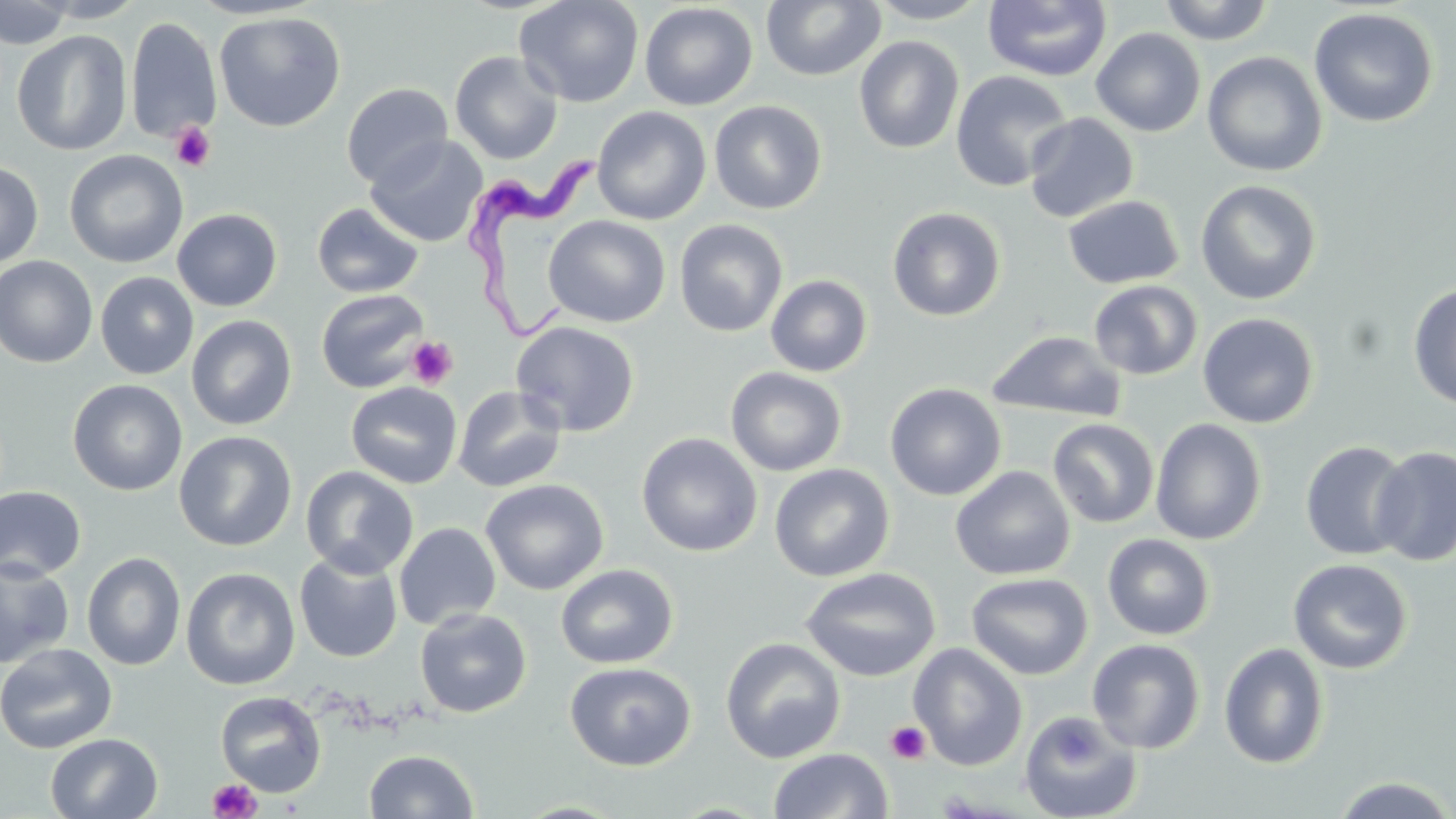
Approximate bounding boxes as named x1/y1/x2/y2 corners in pixels. Platelet locations: (x1=170, y1=121, x2=217, y2=171), (x1=406, y1=337, x2=457, y2=389), (x1=885, y1=720, x2=931, y2=764), (x1=208, y1=778, x2=262, y2=819). Trypanosoma brucei locations: (x1=460, y1=139, x2=609, y2=353). Uninfected red blood cell locations: (x1=0, y1=0, x2=75, y2=49), (x1=32, y1=0, x2=147, y2=23), (x1=514, y1=0, x2=645, y2=108), (x1=760, y1=0, x2=886, y2=82), (x1=865, y1=0, x2=994, y2=25), (x1=982, y1=0, x2=1112, y2=83), (x1=1156, y1=0, x2=1276, y2=45), (x1=639, y1=2, x2=758, y2=111), (x1=1308, y1=6, x2=1439, y2=129), (x1=213, y1=11, x2=346, y2=133), (x1=125, y1=16, x2=222, y2=143), (x1=1091, y1=27, x2=1206, y2=137), (x1=11, y1=30, x2=132, y2=155), (x1=853, y1=35, x2=964, y2=154), (x1=1091, y1=37, x2=1325, y2=154), (x1=450, y1=50, x2=563, y2=163), (x1=1202, y1=51, x2=1327, y2=177), (x1=950, y1=70, x2=1074, y2=192), (x1=341, y1=82, x2=453, y2=189), (x1=709, y1=100, x2=827, y2=214), (x1=592, y1=106, x2=711, y2=225), (x1=1023, y1=113, x2=1139, y2=223), (x1=365, y1=135, x2=487, y2=248), (x1=64, y1=150, x2=188, y2=268), (x1=0, y1=161, x2=43, y2=270), (x1=1195, y1=179, x2=1322, y2=305), (x1=1062, y1=195, x2=1184, y2=289), (x1=311, y1=202, x2=424, y2=298), (x1=887, y1=206, x2=1007, y2=322), (x1=172, y1=208, x2=282, y2=312), (x1=543, y1=215, x2=671, y2=328), (x1=674, y1=219, x2=789, y2=337), (x1=0, y1=256, x2=98, y2=368), (x1=95, y1=272, x2=199, y2=379), (x1=765, y1=274, x2=872, y2=377), (x1=1088, y1=280, x2=1203, y2=381), (x1=1407, y1=283, x2=1456, y2=411), (x1=316, y1=288, x2=430, y2=393), (x1=1197, y1=312, x2=1320, y2=428), (x1=186, y1=315, x2=297, y2=431), (x1=511, y1=320, x2=640, y2=437), (x1=985, y1=330, x2=1127, y2=423), (x1=726, y1=367, x2=847, y2=476), (x1=68, y1=378, x2=187, y2=496), (x1=346, y1=382, x2=463, y2=488), (x1=884, y1=382, x2=1007, y2=501), (x1=452, y1=386, x2=566, y2=493), (x1=1150, y1=417, x2=1267, y2=546), (x1=1047, y1=418, x2=1160, y2=528), (x1=174, y1=430, x2=297, y2=552), (x1=636, y1=432, x2=762, y2=557), (x1=1299, y1=439, x2=1414, y2=561), (x1=1369, y1=445, x2=1456, y2=566), (x1=769, y1=463, x2=895, y2=582), (x1=950, y1=465, x2=1076, y2=581), (x1=301, y1=466, x2=419, y2=579), (x1=480, y1=478, x2=609, y2=595), (x1=0, y1=486, x2=86, y2=582), (x1=394, y1=522, x2=501, y2=631), (x1=1102, y1=534, x2=1215, y2=640), (x1=82, y1=551, x2=186, y2=671), (x1=294, y1=552, x2=403, y2=663), (x1=1287, y1=558, x2=1413, y2=674), (x1=0, y1=559, x2=74, y2=669), (x1=555, y1=564, x2=678, y2=669), (x1=181, y1=567, x2=300, y2=690), (x1=800, y1=567, x2=941, y2=682), (x1=966, y1=572, x2=1093, y2=680), (x1=414, y1=608, x2=532, y2=718), (x1=720, y1=637, x2=846, y2=763), (x1=1086, y1=638, x2=1206, y2=754), (x1=1218, y1=642, x2=1329, y2=769), (x1=0, y1=643, x2=118, y2=754), (x1=908, y1=643, x2=1028, y2=771), (x1=564, y1=662, x2=697, y2=771), (x1=215, y1=690, x2=327, y2=797), (x1=1018, y1=710, x2=1143, y2=819), (x1=45, y1=732, x2=163, y2=819), (x1=768, y1=748, x2=894, y2=818), (x1=364, y1=749, x2=479, y2=818), (x1=1331, y1=775, x2=1455, y2=818). Slide-level diagnosis: Trypanosoma brucei. Image is 1456×819 pixels. Captured at 1000x magnification. Single field of view. May-Grünwald-Giemsa-stained preparation. Thin blood film. Light microscopy.